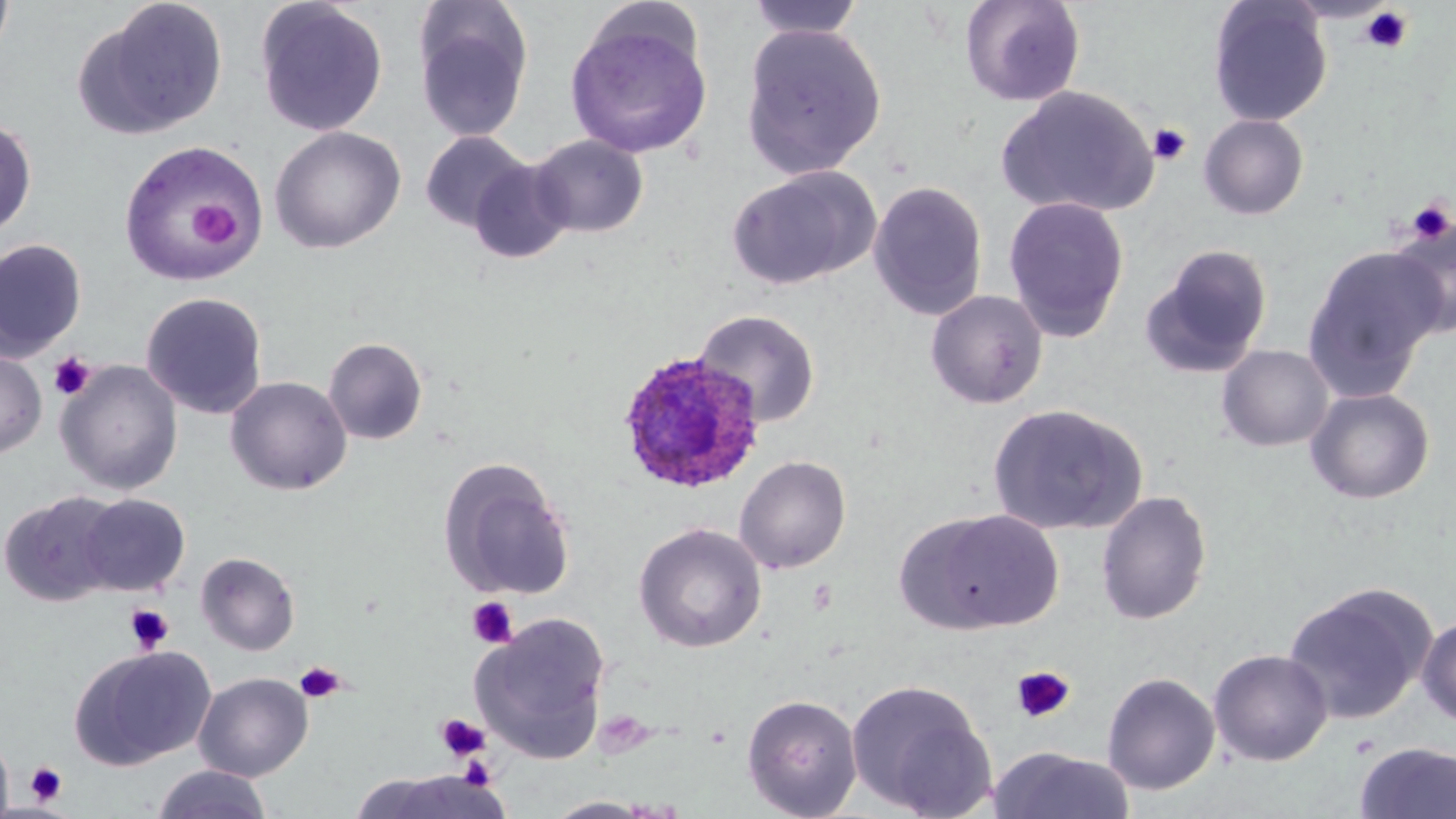

Approximate bounding boxes as (x1,y1)-(x2,y2) corner pairs in pixels. Platelet locations: (1359,6)-(1413,54), (1148,123)-(1191,166), (1406,198)-(1454,245), (190,202)-(239,246), (49,350)-(96,401), (466,597)-(518,649), (124,604)-(174,654), (294,661)-(345,704), (1010,666)-(1075,724), (434,713)-(491,763), (24,762)-(67,806). Uninfected red blood cell locations: (0,0)-(15,62), (76,0)-(229,140), (745,0)-(866,40), (959,0)-(1086,108), (254,1)-(389,137), (1207,1)-(1332,127), (413,2)-(534,143), (565,18)-(714,159), (741,24)-(887,180), (997,85)-(1159,219), (1198,114)-(1310,220), (0,117)-(37,237), (270,126)-(406,254), (420,131)-(531,233), (529,134)-(649,238), (118,141)-(266,285), (467,157)-(574,265), (727,166)-(881,290), (868,180)-(988,321), (1003,195)-(1129,342), (1387,216)-(1455,339), (0,239)-(86,363), (1139,244)-(1274,378), (1302,245)-(1445,399), (925,289)-(1049,409), (140,292)-(268,419), (693,308)-(821,427), (322,337)-(428,445), (1216,344)-(1335,452), (0,349)-(47,458), (56,360)-(183,495), (225,376)-(352,495), (1305,387)-(1435,504), (986,403)-(1148,536), (734,455)-(851,574), (438,457)-(576,602), (1096,490)-(1212,625), (1,492)-(123,605), (77,493)-(190,596), (909,508)-(1065,634), (633,523)-(766,653), (196,551)-(300,655), (1283,582)-(1435,725), (471,612)-(612,763), (1417,614)-(1456,728), (71,645)-(215,768), (1208,649)-(1333,766), (1102,665)-(1332,778), (194,672)-(313,781), (1101,672)-(1220,795), (845,677)-(997,818), (742,694)-(862,818), (0,733)-(14,819), (1354,741)-(1456,819), (989,747)-(1136,819), (152,765)-(274,819), (350,770)-(509,818), (544,796)-(659,818). Plasmodium ovale-infected red blood cell locations: (615,349)-(766,494). Slide-level diagnosis: Plasmodium ovale. 1000x magnification. Light microscopy. Thin blood film. Single field of view. May-Grünwald-Giemsa stain. Image is 1456×819 pixels.